Classify this cell by malaria status.
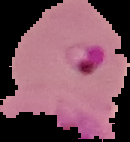

It is parasitized.

image_size: 130×142 pixels
image_type: segmented cell region on a black background
preparation: thin blood smear